Point out each malaria parasite.
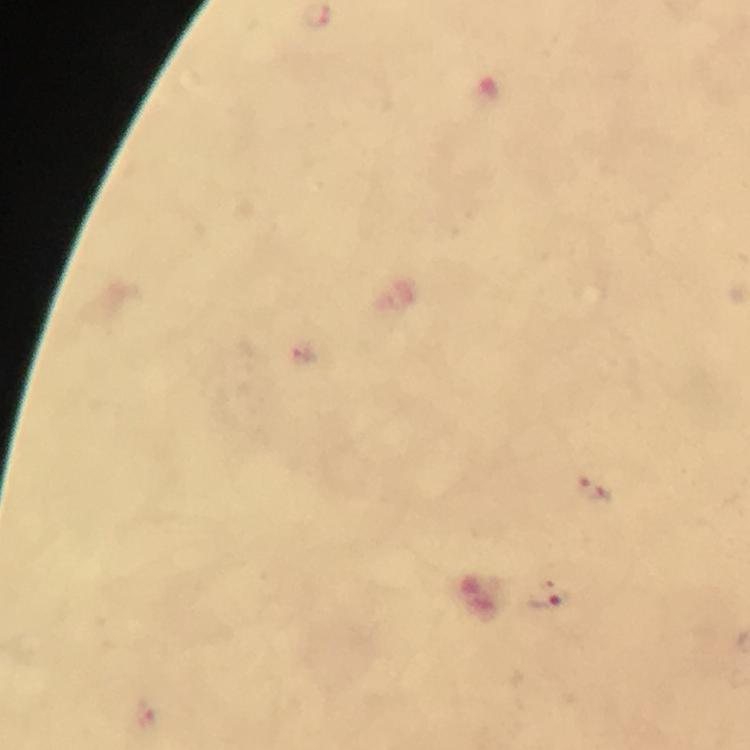

Approximate centers as [x, y] in pixels.
Malaria parasites: [302, 354], [593, 490], [547, 600].

{
  "image_size": "750×750 pixels",
  "magnification": "100x",
  "cropped_from": "a single field of view",
  "context": "from a diagnostic examination for malaria",
  "capture": "smartphone mounted on the microscope",
  "immersion_oil": "used",
  "stain": "Giemsa",
  "preparation": "thick smear"
}